Outline each uninfected red blood cell.
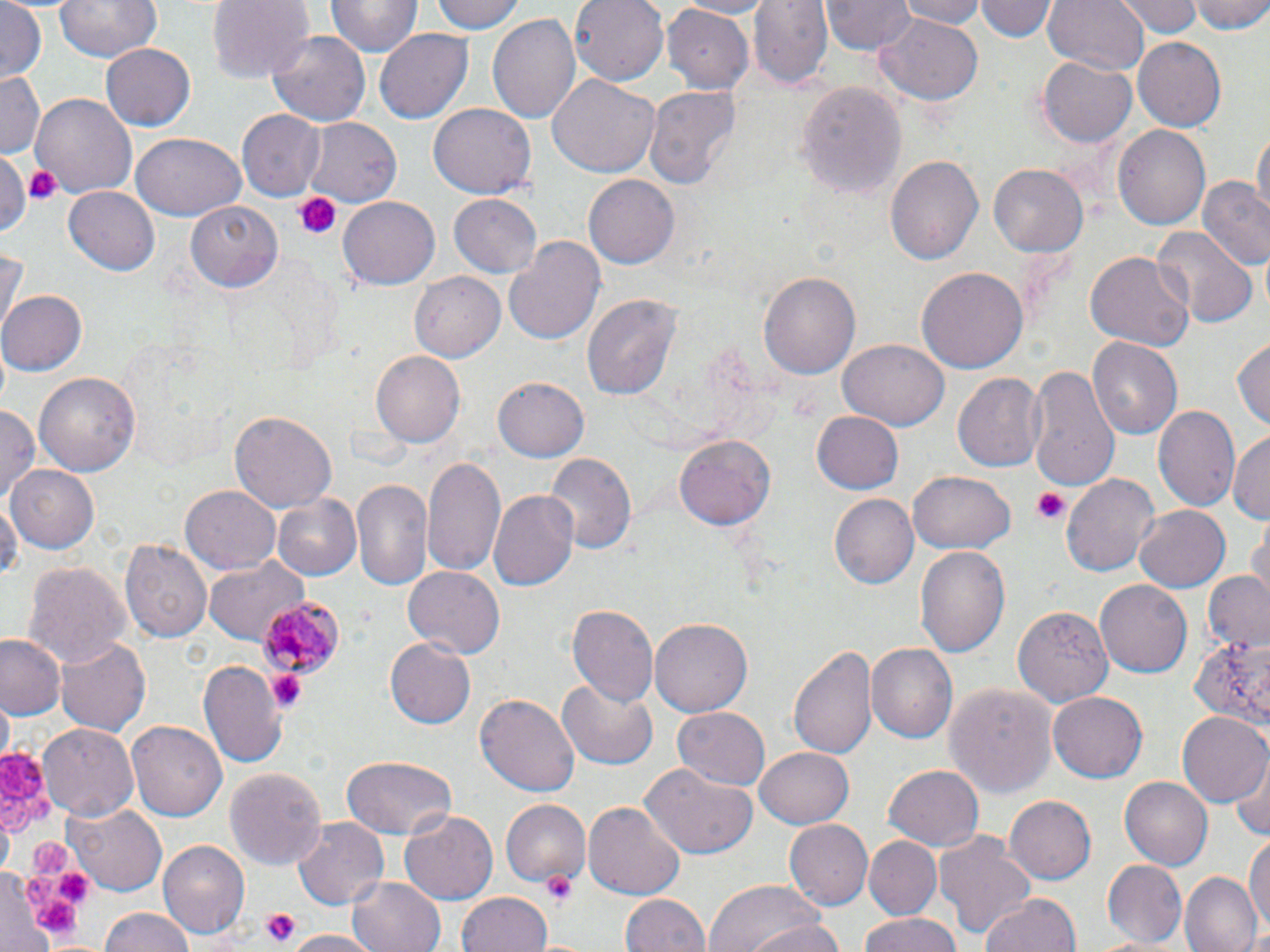

Approximate bounding boxes as (x1,y1)-(x2,y2) corner pairs in pixels.
Uninfected red blood cells: (57,0)-(161,62), (208,0)-(314,85), (426,0)-(523,35), (569,0)-(670,83), (667,0)-(778,17), (748,0)-(831,90), (822,0)-(914,54), (897,0)-(991,27), (976,0)-(1055,43), (1044,0)-(1148,77), (1122,0)-(1201,36), (1190,0)-(1270,35), (326,1)-(420,60), (0,3)-(46,84), (661,7)-(755,93), (485,11)-(581,127), (875,15)-(982,108), (266,29)-(373,128), (375,29)-(471,124), (1134,37)-(1225,132), (100,42)-(196,131), (1038,57)-(1138,148), (0,71)-(45,157), (546,72)-(658,180), (796,78)-(906,196), (643,86)-(741,195), (32,93)-(138,198), (428,103)-(535,198), (237,108)-(325,201), (300,115)-(404,208), (1112,124)-(1211,230), (1253,127)-(1269,222), (128,133)-(247,220), (0,149)-(32,239), (885,155)-(983,264), (989,163)-(1089,258), (583,172)-(679,266), (1199,176)-(1268,271), (65,185)-(162,274), (450,195)-(542,278), (339,196)-(439,291), (187,200)-(281,292), (1152,223)-(1255,328), (505,237)-(604,345), (0,246)-(24,336), (1083,246)-(1194,351), (918,267)-(1027,373), (759,269)-(862,382), (411,271)-(505,362), (0,290)-(84,377), (581,293)-(683,403), (1232,334)-(1270,431), (839,337)-(950,431), (1088,337)-(1181,441), (371,350)-(465,448), (1026,366)-(1120,490), (35,371)-(141,481), (954,371)-(1046,473), (494,376)-(590,463), (0,404)-(40,503), (1154,405)-(1241,513), (809,410)-(904,496), (230,411)-(337,515), (1229,429)-(1270,522), (675,435)-(775,532), (544,453)-(635,557), (423,457)-(507,581), (10,465)-(100,551), (910,470)-(1015,555), (1062,471)-(1160,576), (350,478)-(434,594), (487,484)-(579,591), (182,486)-(280,575), (272,492)-(363,581), (831,494)-(920,590), (1,496)-(20,585), (1133,505)-(1231,593), (1250,520)-(1269,603), (121,539)-(212,642), (914,544)-(1011,661), (202,555)-(309,647), (24,559)-(131,672), (403,567)-(503,659), (1204,571)-(1270,653), (1096,579)-(1191,679), (1015,603)-(1116,708), (567,605)-(657,708), (650,618)-(753,715), (1190,625)-(1270,727), (1,635)-(66,716), (57,637)-(150,736), (385,639)-(475,727), (789,640)-(881,764), (867,644)-(957,745), (199,661)-(286,766), (557,675)-(660,770), (942,681)-(1057,801), (475,692)-(579,797), (1049,693)-(1148,782), (672,707)-(770,791), (1179,712)-(1269,808), (129,722)-(226,822), (39,726)-(137,823), (753,746)-(852,828), (342,755)-(457,837), (1230,755)-(1270,844), (641,765)-(757,861), (884,765)-(982,852), (227,767)-(326,874), (1118,773)-(1213,868), (1006,795)-(1097,885), (500,799)-(591,885), (581,802)-(685,901), (67,803)-(167,895), (400,810)-(497,903), (293,818)-(387,909), (787,818)-(873,909), (1245,827)-(1270,942), (934,833)-(1038,941), (864,837)-(940,921), (159,840)-(249,940), (1103,860)-(1185,943), (1183,872)-(1262,952), (347,874)-(448,952), (707,879)-(830,952), (979,891)-(1081,952), (456,892)-(551,952), (621,893)-(709,952), (98,910)-(196,952), (739,915)-(848,952), (855,916)-(966,952), (287,932)-(378,952).

Platelet locations: (25,165)-(61,206), (294,192)-(342,240), (1031,490)-(1069,525), (268,671)-(307,710), (0,750)-(46,804), (1,795)-(33,837), (26,795)-(55,823), (31,839)-(71,879), (543,871)-(576,906), (21,873)-(62,908), (53,873)-(91,903), (34,895)-(79,933), (258,908)-(302,948). Plasmodium malariae-infected red blood cell locations: (257,596)-(340,679). Slide-level diagnosis: Plasmodium malariae. One field of a larger specimen. May-Grünwald-Giemsa stain. Image is 1270×952 pixels. Optical microscopy. Thin blood film. 1000x magnification.